Locate every Plasmodium vivax-infected red blood cell.
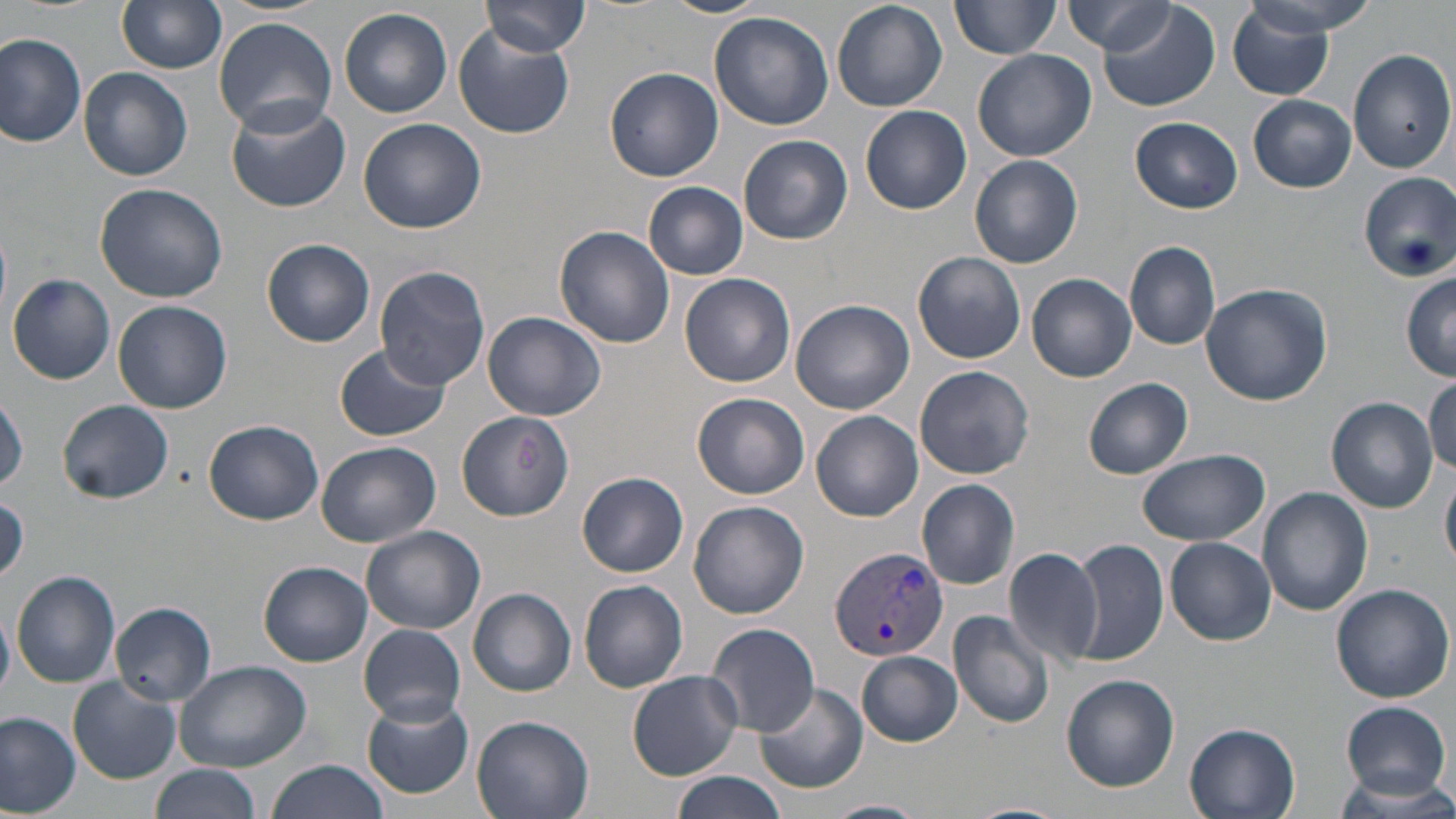

Approximate bounding boxes as (x1, y1, x2, y2) in pixels.
Plasmodium vivax-infected red blood cells: (828, 544, 949, 662).

Uninfected red blood cell locations: (117, 0, 228, 73), (662, 0, 764, 18), (830, 0, 948, 114), (950, 0, 1060, 59), (1234, 0, 1377, 46), (480, 1, 591, 59), (1060, 1, 1177, 53), (1096, 1, 1221, 112), (1227, 3, 1345, 100), (339, 7, 452, 118), (708, 12, 834, 130), (213, 16, 337, 135), (453, 29, 575, 139), (0, 33, 88, 149), (1348, 48, 1456, 174), (971, 49, 1096, 163), (79, 67, 193, 181), (604, 67, 723, 182), (1248, 94, 1356, 193), (225, 99, 351, 212), (860, 105, 972, 215), (1131, 116, 1243, 213), (358, 118, 486, 234), (738, 134, 853, 245), (970, 155, 1082, 270), (1357, 172, 1456, 282), (93, 182, 227, 303), (645, 182, 749, 279), (555, 225, 675, 350), (262, 238, 376, 346), (1125, 241, 1222, 350), (914, 252, 1027, 364), (374, 265, 491, 389), (1398, 270, 1453, 378), (679, 272, 796, 387), (1027, 272, 1138, 382), (8, 273, 116, 385), (1200, 282, 1332, 406), (790, 299, 914, 414), (113, 300, 234, 415), (482, 311, 606, 421), (335, 344, 450, 442), (915, 365, 1035, 477), (1425, 375, 1456, 470), (1084, 377, 1194, 479), (692, 393, 810, 499), (1, 394, 26, 493), (1326, 397, 1438, 514), (57, 399, 174, 504), (457, 410, 575, 522), (812, 410, 923, 522), (204, 420, 323, 525), (315, 440, 439, 547), (1135, 449, 1270, 546), (1442, 466, 1456, 572), (577, 473, 689, 577), (917, 478, 1020, 589), (1257, 487, 1373, 616), (688, 500, 809, 619), (361, 525, 486, 636), (1166, 538, 1276, 646), (1069, 540, 1167, 666), (1003, 547, 1104, 666), (259, 561, 372, 666), (12, 571, 119, 688), (969, 572, 1079, 705), (577, 578, 689, 693), (1330, 581, 1455, 702), (468, 587, 576, 696), (112, 601, 215, 704), (0, 604, 15, 700), (948, 608, 1056, 728), (706, 622, 820, 736), (358, 624, 468, 726), (857, 651, 962, 746), (173, 660, 313, 769), (629, 670, 742, 780), (1062, 674, 1180, 792), (68, 677, 181, 783), (754, 682, 869, 795), (361, 694, 473, 799), (1339, 699, 1454, 799), (0, 709, 81, 814), (472, 714, 596, 819), (1184, 724, 1300, 819), (263, 760, 393, 819), (148, 765, 260, 819), (670, 772, 789, 819), (1329, 772, 1456, 815), (824, 798, 930, 819), (957, 801, 1069, 819). Slide-level diagnosis: Plasmodium vivax. Captured at 1000x magnification. Thin blood smear. Image is 1456×819 pixels. Single field of view. Optical microscopy. May-Grünwald-Giemsa-stained preparation.